Report the malaria status of this cell.
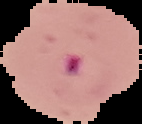
Parasitized.

Summary:
  - Preparation: thin blood smear
  - Image type: cell region segmented out of the field of view; surrounding area masked to black
  - Image size: 142×124 pixels